Name the parasite shown.
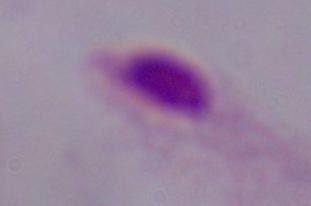
This is a trichomonad.

1000x magnification. Photomicrograph.